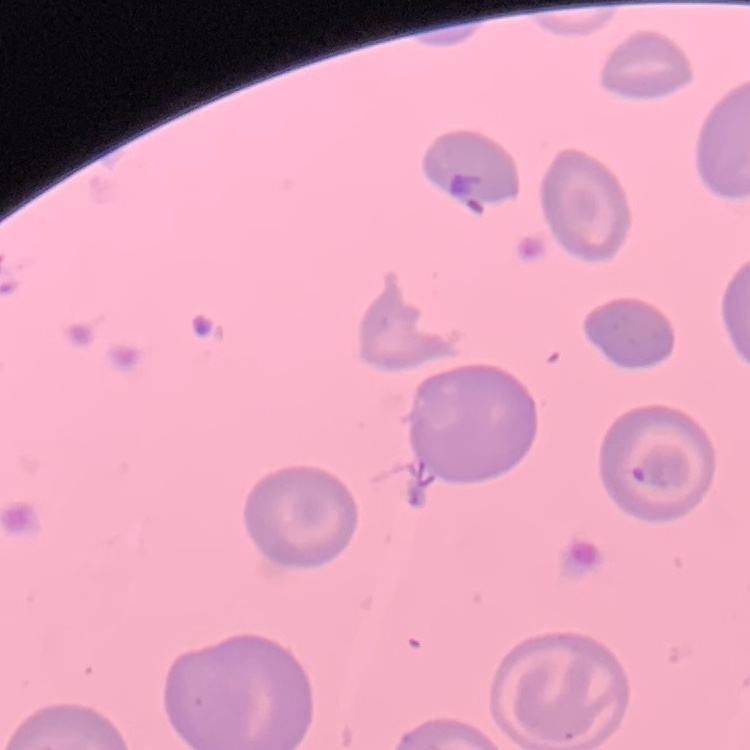

{
  "erythrocyte_morphology": "no rouleaux formation",
  "image_type": "one tile cut from a larger photomicrograph",
  "stain": "Field's or Giemsa",
  "preparation": "thin blood film"
}